State the preparation type.
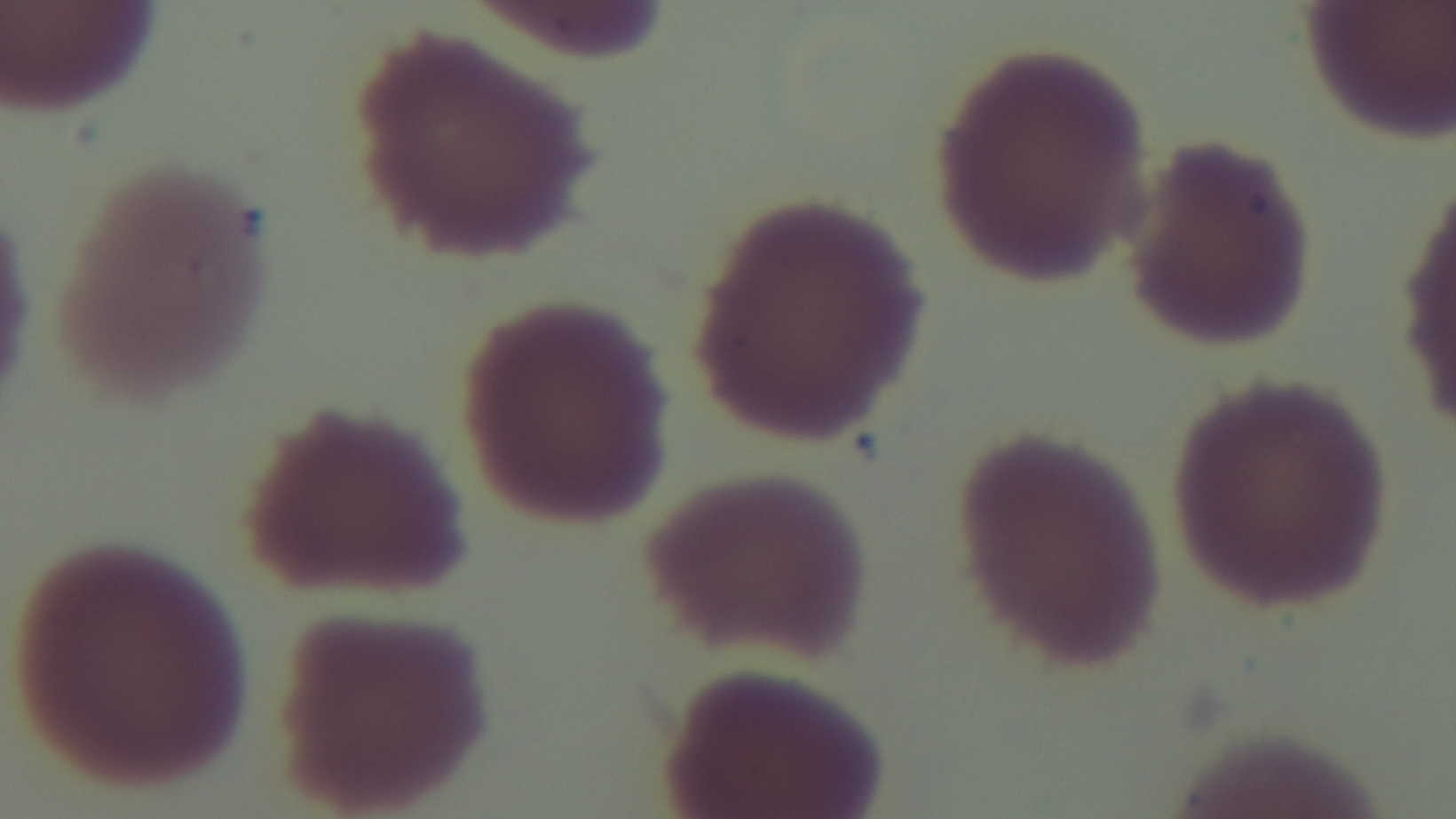

A thin smear.

capture = mounted 4K digital camera
field of view = single
objective = 100x oil immersion
stain = Giemsa
malaria status = uninfected
modality = light microscopy